Describe the morphology of the red blood cells.
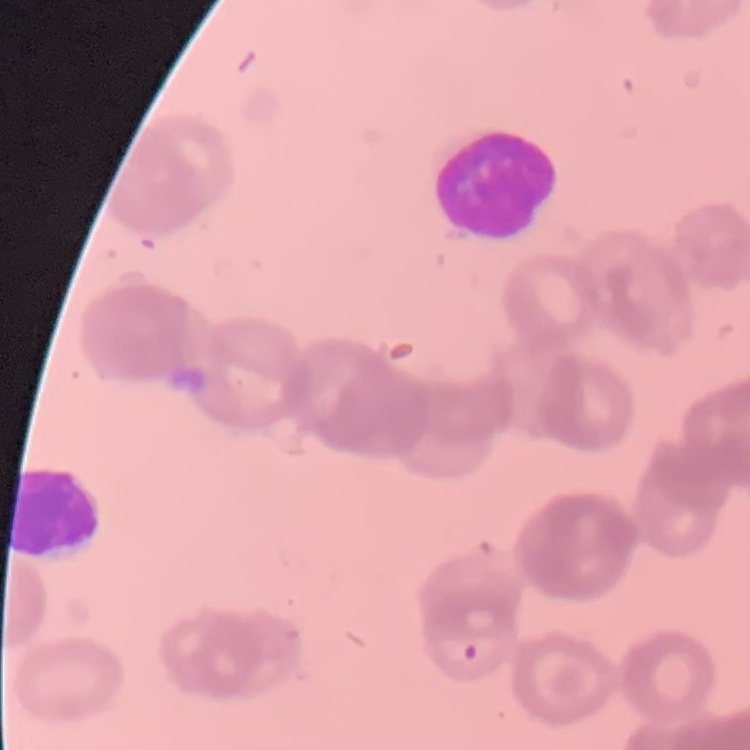

They show rouleaux formation.

stain = Field's or Giemsa
image type = square crop of a larger photomicrograph
preparation = thin blood film